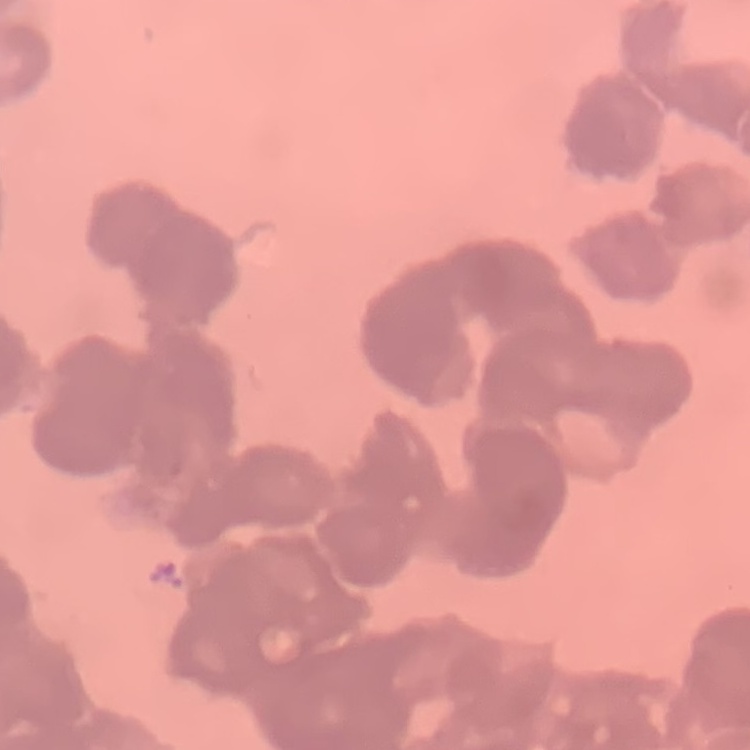
The red blood cells exhibit rouleaux formation. Square crop of a larger photomicrograph. Field's or Giemsa stain. Thin blood film.